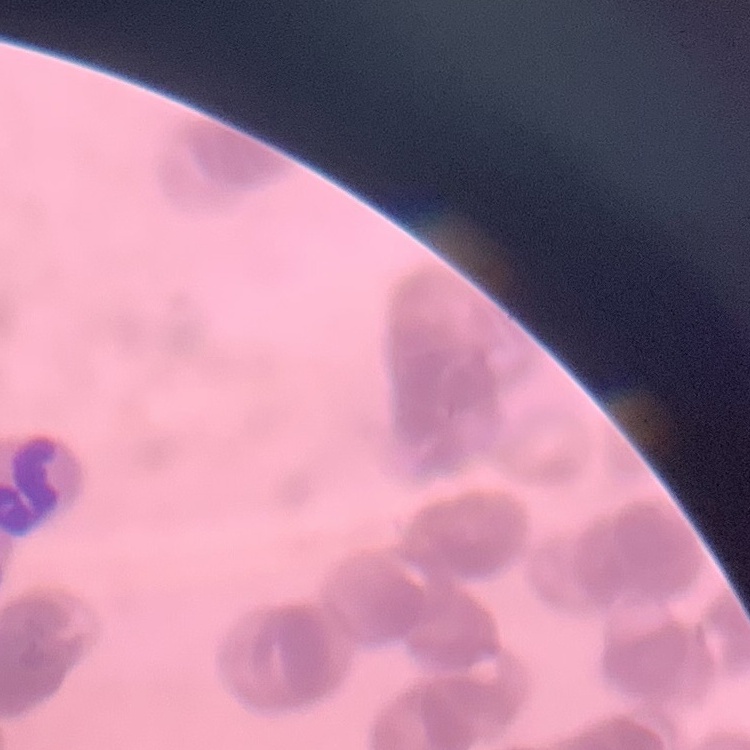 The erythrocytes exhibit rouleaux formation. Stained with either Field's or Giemsa. Thin peripheral smear. Square crop of a larger photomicrograph.